Locate and identify every blood parasite.
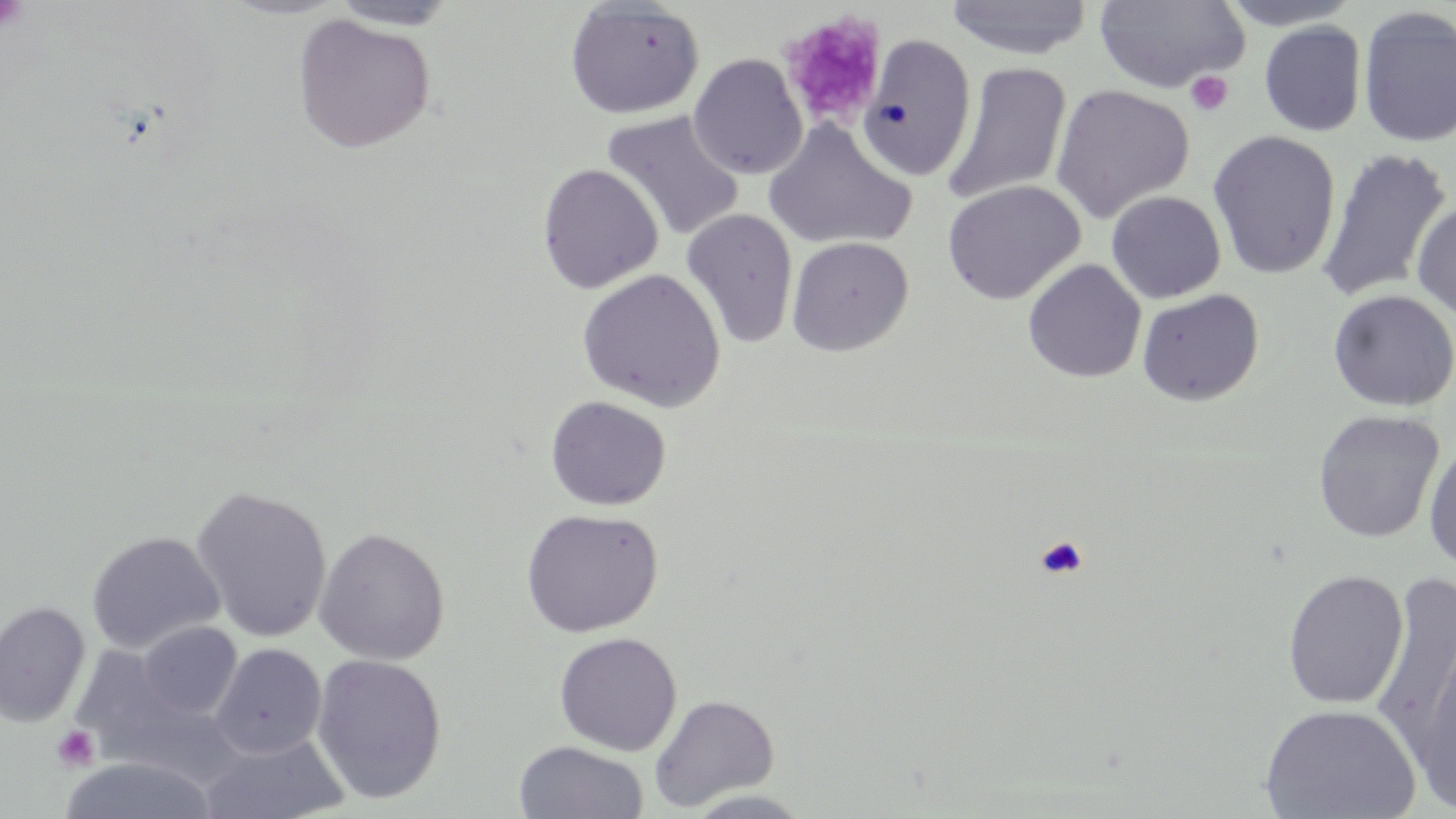

No blood parasites observed.

Approximate bounding boxes as named x1/y1/x2/y2 corners in pixels. Uninfected red blood cell locations: (x1=944, y1=0, x2=1094, y2=60), (x1=1214, y1=0, x2=1365, y2=30), (x1=327, y1=1, x2=464, y2=31), (x1=564, y1=1, x2=705, y2=119), (x1=1093, y1=1, x2=1250, y2=93), (x1=1357, y1=5, x2=1456, y2=149), (x1=293, y1=13, x2=436, y2=154), (x1=1259, y1=21, x2=1367, y2=137), (x1=858, y1=34, x2=977, y2=182), (x1=688, y1=53, x2=809, y2=180), (x1=943, y1=62, x2=1072, y2=207), (x1=1050, y1=83, x2=1194, y2=223), (x1=601, y1=109, x2=746, y2=242), (x1=763, y1=118, x2=917, y2=251), (x1=1207, y1=130, x2=1341, y2=280), (x1=1316, y1=147, x2=1454, y2=305), (x1=537, y1=162, x2=664, y2=294), (x1=942, y1=179, x2=1085, y2=305), (x1=1105, y1=191, x2=1226, y2=303), (x1=1411, y1=198, x2=1456, y2=321), (x1=680, y1=208, x2=799, y2=349), (x1=786, y1=236, x2=914, y2=356), (x1=1023, y1=258, x2=1146, y2=383), (x1=576, y1=268, x2=726, y2=412), (x1=1136, y1=289, x2=1264, y2=406), (x1=1328, y1=289, x2=1455, y2=412), (x1=545, y1=395, x2=672, y2=511), (x1=1312, y1=410, x2=1445, y2=544), (x1=1423, y1=438, x2=1456, y2=573), (x1=189, y1=485, x2=333, y2=642), (x1=520, y1=507, x2=663, y2=637), (x1=312, y1=527, x2=450, y2=665), (x1=86, y1=531, x2=225, y2=654), (x1=1282, y1=569, x2=1409, y2=709), (x1=1371, y1=571, x2=1456, y2=762), (x1=0, y1=600, x2=91, y2=727), (x1=135, y1=621, x2=242, y2=720), (x1=1414, y1=629, x2=1456, y2=817), (x1=554, y1=632, x2=682, y2=756), (x1=209, y1=643, x2=327, y2=759), (x1=73, y1=653, x2=236, y2=792), (x1=310, y1=653, x2=448, y2=805), (x1=648, y1=693, x2=779, y2=812), (x1=1260, y1=703, x2=1422, y2=818), (x1=197, y1=732, x2=351, y2=819), (x1=513, y1=740, x2=649, y2=819), (x1=56, y1=756, x2=218, y2=818), (x1=679, y1=789, x2=816, y2=818). Platelet locations: (x1=0, y1=0, x2=30, y2=33), (x1=780, y1=11, x2=887, y2=128), (x1=1185, y1=70, x2=1233, y2=116), (x1=1034, y1=534, x2=1089, y2=580), (x1=51, y1=724, x2=100, y2=772). Slide-level diagnosis: no evidence of blood parasites. May-Grünwald-Giemsa stain. Captured at 1000x magnification. Optical microscopy. Thin blood film. Single field of view. Image is 1456×819 pixels.